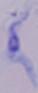 1000x magnification. A trypanosome is shown. Micrograph.